Assess this cell for malaria.
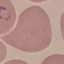
It is parasitized.

Summary:
  - Capture: smartphone through the microscope eyepiece
  - Image type: cell patch, automatically extracted from a larger field of view and resized to 64 × 64 pixels
  - Stain: Giemsa
  - Preparation: thin smear